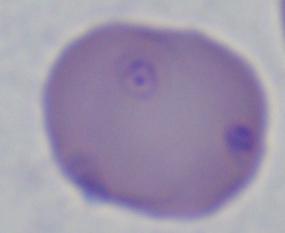 1000x magnification. A Babesia parasite is shown. Micrograph.